Outline each blood parasite and name the species.
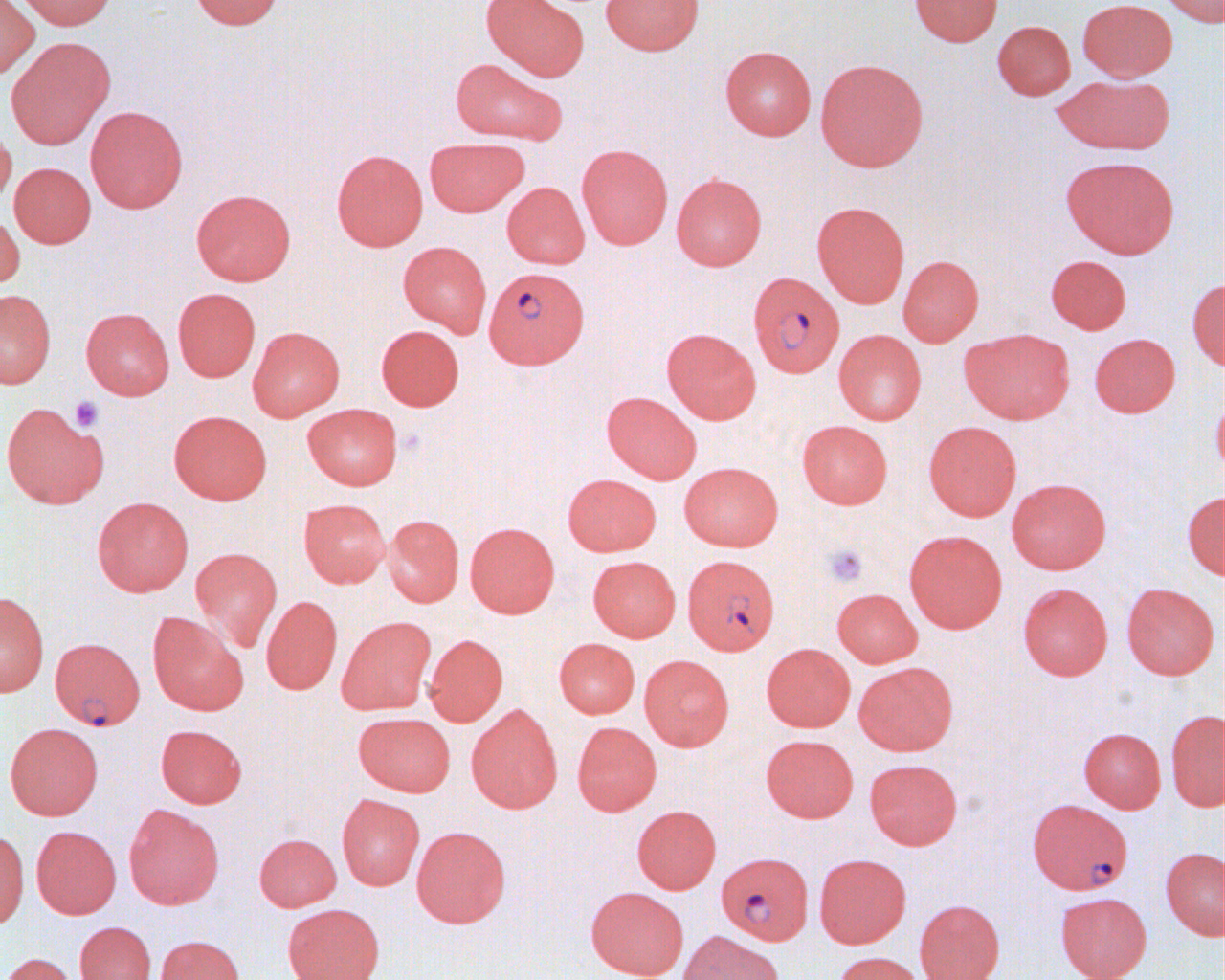
Approximate bounding boxes as (x1,y1)-(x2,y2) corner pairs in pixels.
Plasmodium falciparum-infected red blood cells: (483,266)-(589,369), (748,272)-(844,377), (683,555)-(780,655), (49,637)-(145,731), (1028,798)-(1132,894), (720,857)-(813,948).
No Plasmodium ovale, Plasmodium malariae, Plasmodium vivax, Babesia divergens, or Trypanosoma brucei observed.

Summary:
  - Platelet locations: (69,396)-(104,432), (823,544)-(868,587)
  - Uninfected red blood cell locations: (0,0)-(39,79), (15,0)-(116,30), (189,0)-(283,30), (481,0)-(589,81), (600,0)-(704,55), (908,0)-(1003,46), (1077,0)-(1178,81), (1159,0)-(1223,26), (992,20)-(1075,100), (5,36)-(115,149), (720,45)-(816,140), (450,58)-(567,146), (815,58)-(928,172), (1053,74)-(1174,154), (85,105)-(188,213), (0,123)-(16,210), (424,138)-(529,216), (576,144)-(673,249), (332,149)-(428,251), (1062,156)-(1179,258), (9,162)-(96,248), (671,173)-(767,271), (502,182)-(590,269), (191,189)-(296,285), (812,201)-(910,308), (0,211)-(25,291), (398,241)-(492,336), (898,255)-(984,346), (1046,255)-(1131,334), (1187,277)-(1224,371), (173,288)-(261,382), (0,289)-(56,388), (81,307)-(174,400), (376,325)-(464,411), (248,326)-(345,420), (662,328)-(761,424), (834,329)-(926,425), (960,329)-(1074,424), (1089,333)-(1181,417), (602,391)-(701,483), (1212,392)-(1224,485), (1,402)-(108,508), (302,403)-(403,490), (168,410)-(272,504), (796,420)-(893,509), (924,421)-(1022,521), (679,462)-(783,551), (562,474)-(661,556), (1006,478)-(1111,574), (1182,490)-(1225,580), (92,496)-(194,596), (298,498)-(391,587), (383,514)-(464,607), (465,522)-(560,618), (904,530)-(1007,633), (190,547)-(282,651), (587,555)-(680,642), (1018,582)-(1113,680), (1122,583)-(1219,680), (832,588)-(922,667), (0,591)-(49,696), (261,595)-(342,695), (148,612)-(248,715), (336,616)-(436,714), (424,633)-(507,726), (554,638)-(640,718), (761,643)-(855,732), (639,654)-(734,750), (854,661)-(957,756), (466,704)-(563,813), (1166,709)-(1225,811), (353,712)-(456,796), (572,721)-(662,816), (5,723)-(103,820), (156,724)-(247,808), (1079,727)-(1166,813), (762,735)-(858,822), (864,759)-(963,849), (337,793)-(425,890), (123,803)-(224,909), (632,805)-(721,894), (31,825)-(121,918), (411,825)-(511,928), (0,830)-(29,929), (254,833)-(342,911), (1161,848)-(1225,940), (814,853)-(911,948), (586,886)-(688,980), (1055,892)-(1152,980), (914,899)-(1004,980), (283,903)-(384,980), (75,921)-(156,980), (678,931)-(783,980), (155,935)-(245,980), (831,951)-(926,980), (1,952)-(77,980)
  - Slide-level diagnosis: Plasmodium falciparum
  - Modality: light microscopy
  - Preparation: thin blood smear
  - Image size: 1225×980 pixels
  - Magnification: 1000x
  - Field of view: one of a larger specimen